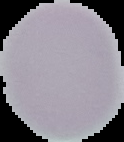

Summary:
  - Result: negative for malaria parasites
  - Image size: 124×142 pixels
  - Preparation: thin blood smear
  - Image type: cell region segmented out of the field of view; surrounding area masked to black